Locate every blood parasite and identify its species.
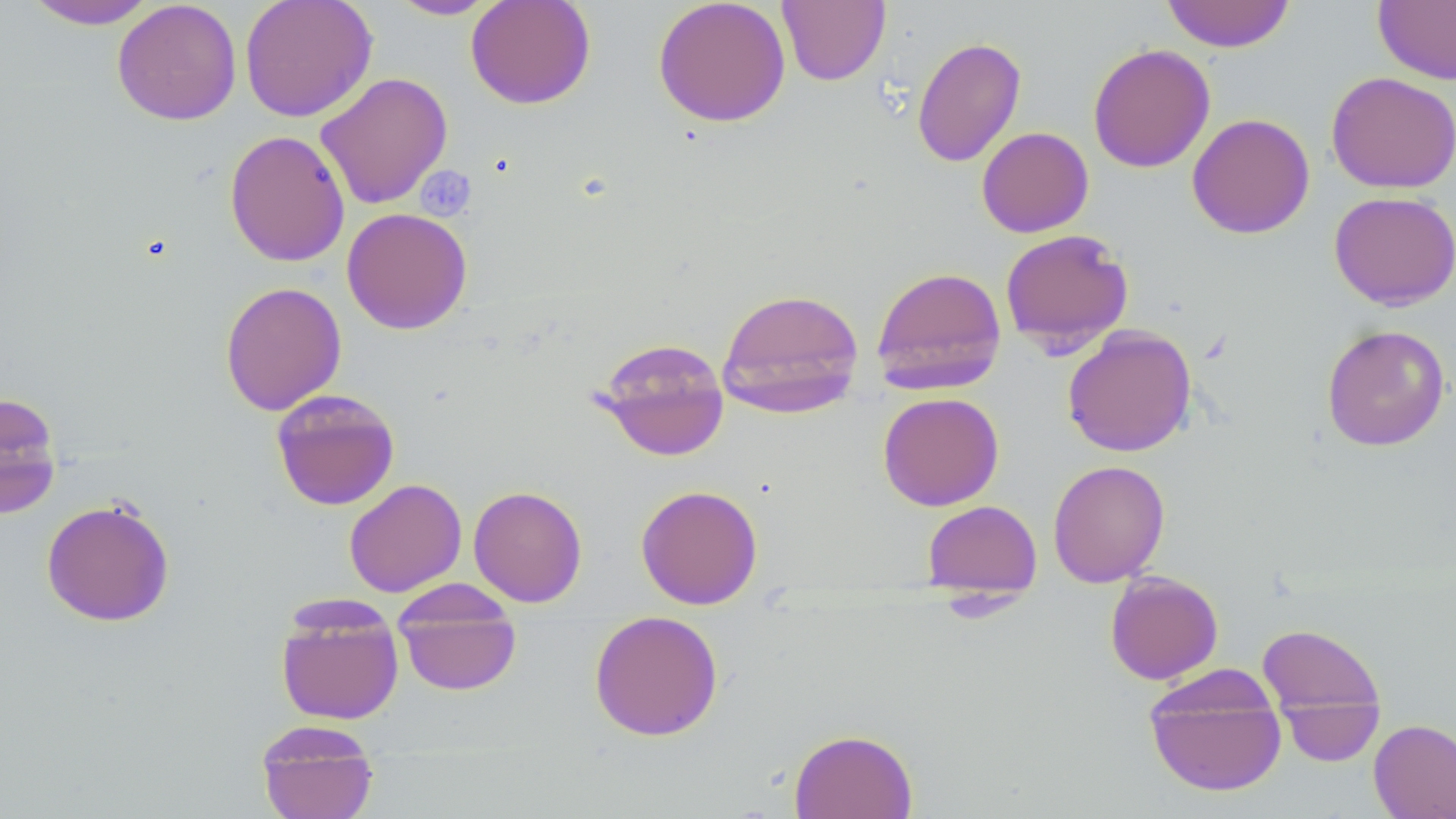

No blood parasites observed.

Summary:
  - Coordinate format: approximate bounding boxes as named x1/y1/x2/y2 corners in pixels
  - Uninfected red blood cell locations: (x1=22, y1=0, x2=161, y2=29), (x1=112, y1=0, x2=242, y2=126), (x1=239, y1=0, x2=377, y2=122), (x1=388, y1=0, x2=500, y2=20), (x1=465, y1=0, x2=596, y2=109), (x1=652, y1=0, x2=791, y2=127), (x1=777, y1=0, x2=890, y2=86), (x1=1161, y1=0, x2=1295, y2=53), (x1=1373, y1=0, x2=1456, y2=85), (x1=912, y1=36, x2=1026, y2=168), (x1=1088, y1=43, x2=1216, y2=173), (x1=315, y1=71, x2=453, y2=210), (x1=1326, y1=71, x2=1456, y2=194), (x1=1187, y1=113, x2=1315, y2=239), (x1=976, y1=127, x2=1093, y2=238), (x1=224, y1=129, x2=350, y2=267), (x1=1328, y1=191, x2=1456, y2=309), (x1=342, y1=207, x2=472, y2=335), (x1=999, y1=229, x2=1134, y2=355), (x1=870, y1=265, x2=1007, y2=395), (x1=220, y1=281, x2=347, y2=416), (x1=717, y1=287, x2=865, y2=416), (x1=1321, y1=324, x2=1450, y2=452), (x1=1062, y1=325, x2=1197, y2=457), (x1=593, y1=336, x2=730, y2=462), (x1=271, y1=388, x2=400, y2=511), (x1=0, y1=391, x2=63, y2=518), (x1=877, y1=392, x2=1004, y2=511), (x1=1047, y1=459, x2=1169, y2=587), (x1=343, y1=478, x2=467, y2=597), (x1=635, y1=484, x2=763, y2=610), (x1=468, y1=485, x2=588, y2=607), (x1=41, y1=498, x2=175, y2=627), (x1=922, y1=500, x2=1042, y2=599), (x1=1105, y1=570, x2=1223, y2=684), (x1=393, y1=594, x2=522, y2=696), (x1=275, y1=601, x2=404, y2=725), (x1=588, y1=610, x2=724, y2=742), (x1=1256, y1=623, x2=1385, y2=724), (x1=1144, y1=667, x2=1287, y2=797), (x1=1279, y1=696, x2=1384, y2=767), (x1=1369, y1=719, x2=1456, y2=819), (x1=255, y1=720, x2=379, y2=819), (x1=788, y1=728, x2=918, y2=819)
  - Slide-level diagnosis: no evidence of blood parasites
  - Preparation: thin blood smear
  - Stain: May-Grünwald-Giemsa
  - Magnification: 1000x
  - Field of view: single
  - Modality: light microscopy
  - Image size: 1456×819 pixels